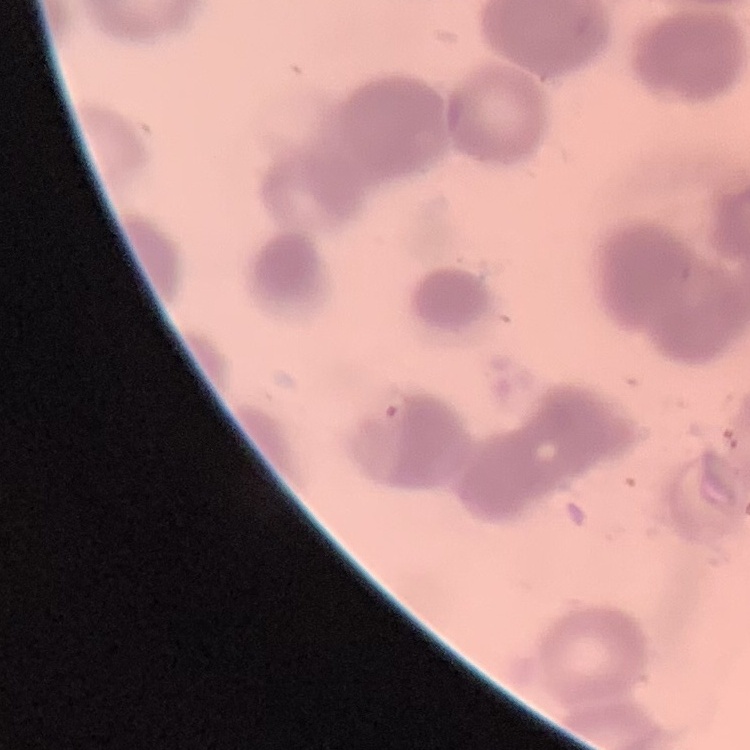
Summary:
  - Red blood cell morphology: rouleaux formation
  - Preparation: thin blood smear
  - Image type: one tile cut from a larger photomicrograph
  - Stain: Field's or Giemsa